Outline each P. falciparum parasite and classify it by life-cycle stage.
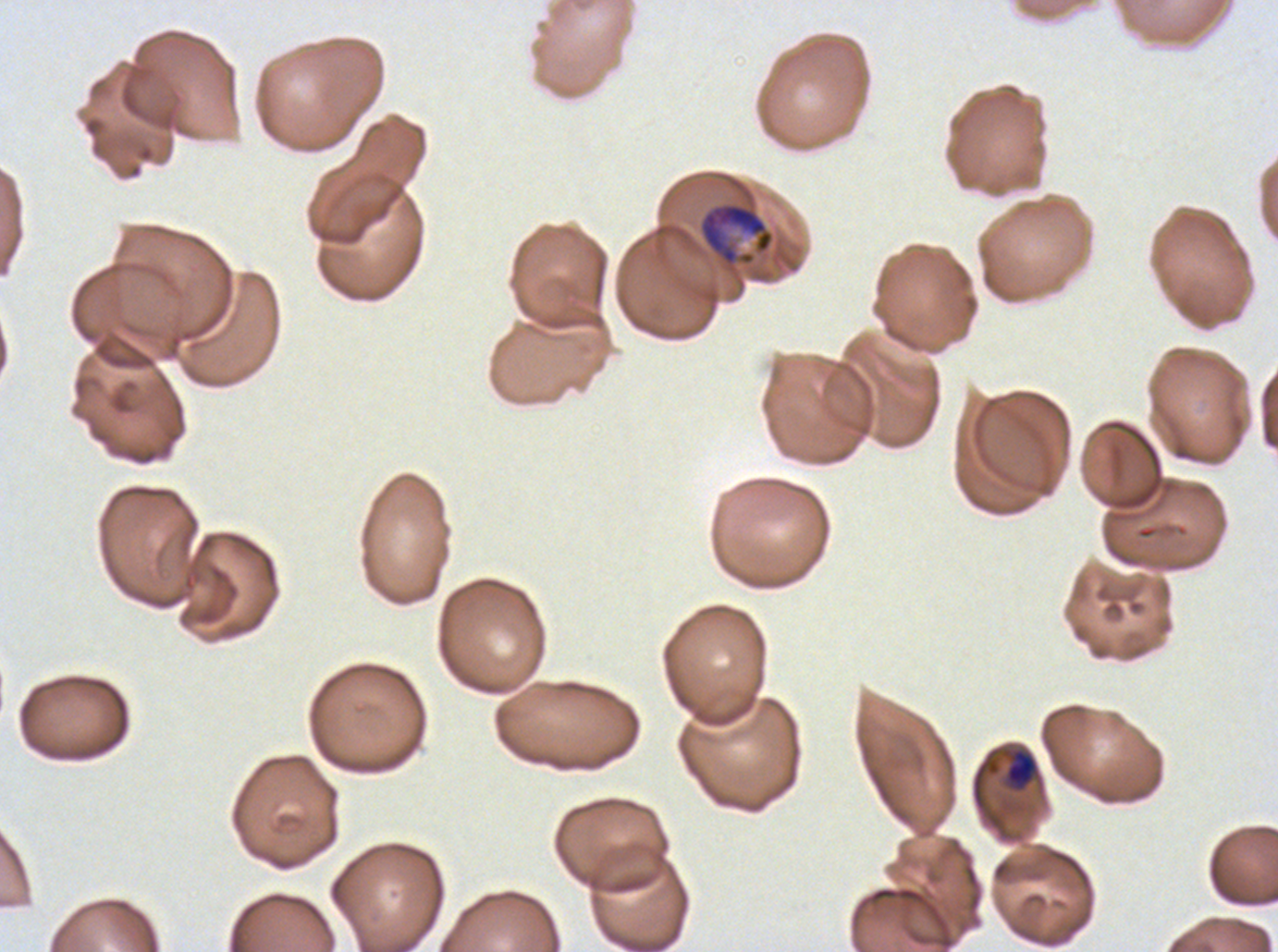

Approximate bounding boxes as (x1, y1, x2, y2) in pixels.
Mid trophozoites: (1004, 747, 1038, 791).
Late trophozoites: (698, 202, 774, 266).
No rings, late-ring/early-trophozoite forms, early schizonts, late schizonts, segmenters, or gametocytes observed.

Thin blood film. Image is 1278×952 pixels. Life-cycle stages observed: mid trophozoite, late trophozoite. Ex-vivo P. falciparum culture from a patient in The Gambia, grown for 24 to 48 hours. One sub-image of a larger composite. Giemsa-stained preparation.